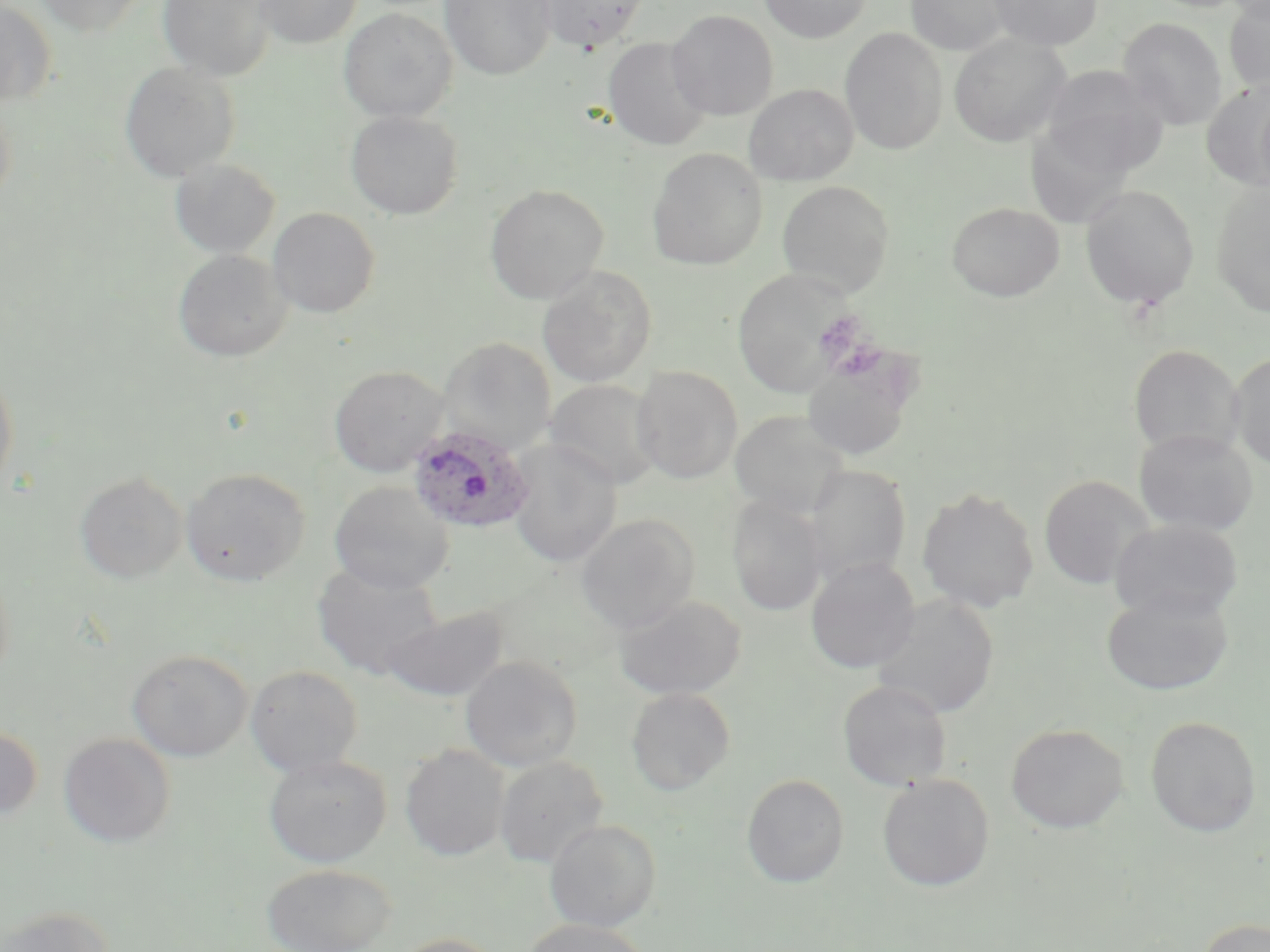
slide-level diagnosis = Plasmodium ovale
magnification = 1000x
image size = 1270×952 pixels
preparation = thin blood film
stain = May-Grünwald-Giemsa
Plasmodium ovale-infected red blood cell locations = approximate bounding boxes as [x1, y1, x2, y2] in pixels: [406, 424, 536, 535]
uninfected red blood cell locations = approximate bounding boxes as [x1, y1, x2, y2] in pixels: [34, 0, 148, 35], [157, 0, 275, 81], [252, 0, 362, 48], [440, 0, 556, 80], [535, 0, 651, 53], [759, 0, 871, 43], [904, 0, 1016, 55], [988, 0, 1102, 50], [1224, 0, 1270, 96], [0, 2, 56, 109], [339, 7, 457, 122], [667, 9, 778, 120], [1117, 17, 1228, 130], [839, 28, 948, 155], [949, 33, 1071, 147], [603, 37, 712, 151], [119, 60, 241, 183], [1039, 65, 1169, 176], [1202, 83, 1270, 189], [743, 84, 859, 186], [0, 93, 16, 212], [345, 110, 463, 219], [647, 146, 768, 270], [170, 158, 280, 258], [776, 180, 895, 296], [1211, 181, 1270, 317], [485, 184, 609, 304], [1080, 184, 1199, 311], [947, 201, 1064, 302], [268, 207, 380, 318], [173, 249, 291, 362], [537, 265, 657, 387], [732, 268, 853, 397], [438, 337, 555, 455], [1129, 345, 1242, 458], [1229, 353, 1270, 469], [801, 357, 914, 460], [0, 366, 18, 499], [329, 366, 449, 477], [631, 366, 743, 484], [545, 379, 662, 490], [730, 410, 849, 517], [1134, 428, 1258, 537], [508, 440, 622, 568], [803, 464, 911, 583], [180, 467, 310, 586], [75, 471, 188, 583], [1038, 475, 1154, 590], [329, 480, 453, 594], [917, 486, 1039, 614], [727, 495, 829, 616], [576, 514, 700, 634], [1110, 519, 1243, 622], [806, 557, 920, 674], [312, 563, 442, 680], [1100, 587, 1234, 696], [611, 593, 748, 701], [870, 595, 1000, 719], [382, 606, 507, 702], [127, 648, 253, 761], [460, 655, 583, 772], [245, 664, 363, 776], [838, 680, 953, 791], [626, 688, 736, 795], [1145, 715, 1261, 837], [1006, 723, 1128, 833], [0, 724, 43, 824], [58, 733, 176, 848], [400, 744, 510, 861], [263, 754, 392, 867], [494, 755, 608, 868], [741, 773, 850, 887], [877, 774, 995, 891], [545, 819, 661, 932], [262, 863, 397, 952], [1, 905, 115, 952], [1198, 918, 1270, 952], [519, 919, 654, 952], [386, 933, 507, 952]
field of view = one of a larger specimen
modality = optical microscopy